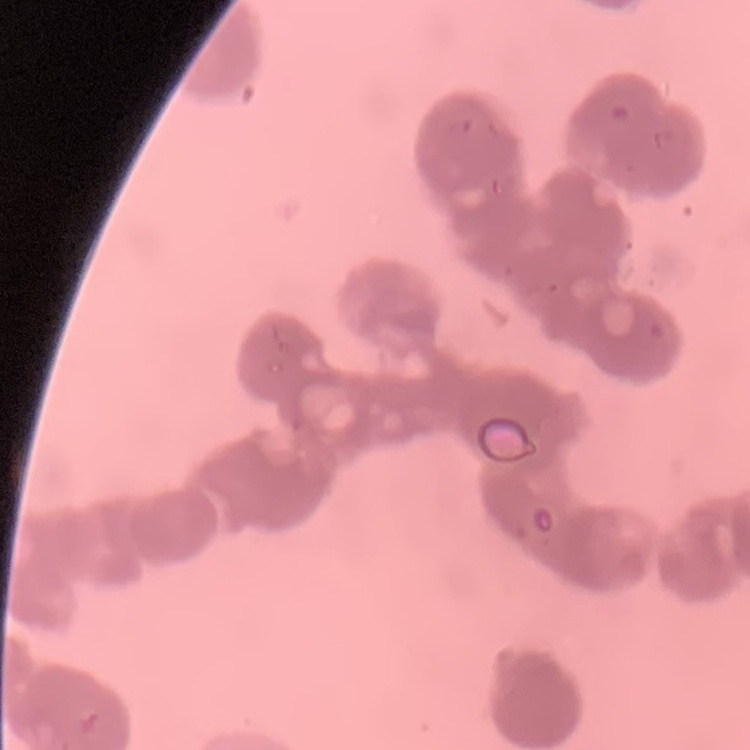

erythrocyte_morphology: rouleaux formation
image_type: one tile cut from a larger photomicrograph
stain: Field's or Giemsa
preparation: thin peripheral smear